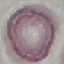
Summary:
  - Result: negative for malaria parasites
  - Stain: Giemsa
  - Capture: smartphone through the microscope eyepiece
  - Preparation: thin smear
  - Image type: automatically extracted cell patch, resized to 64 × 64 pixels